Identify the cell.
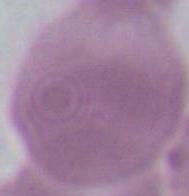

An erythrocyte.

Summary:
  - Magnification: 1000x
  - Modality: photomicrograph